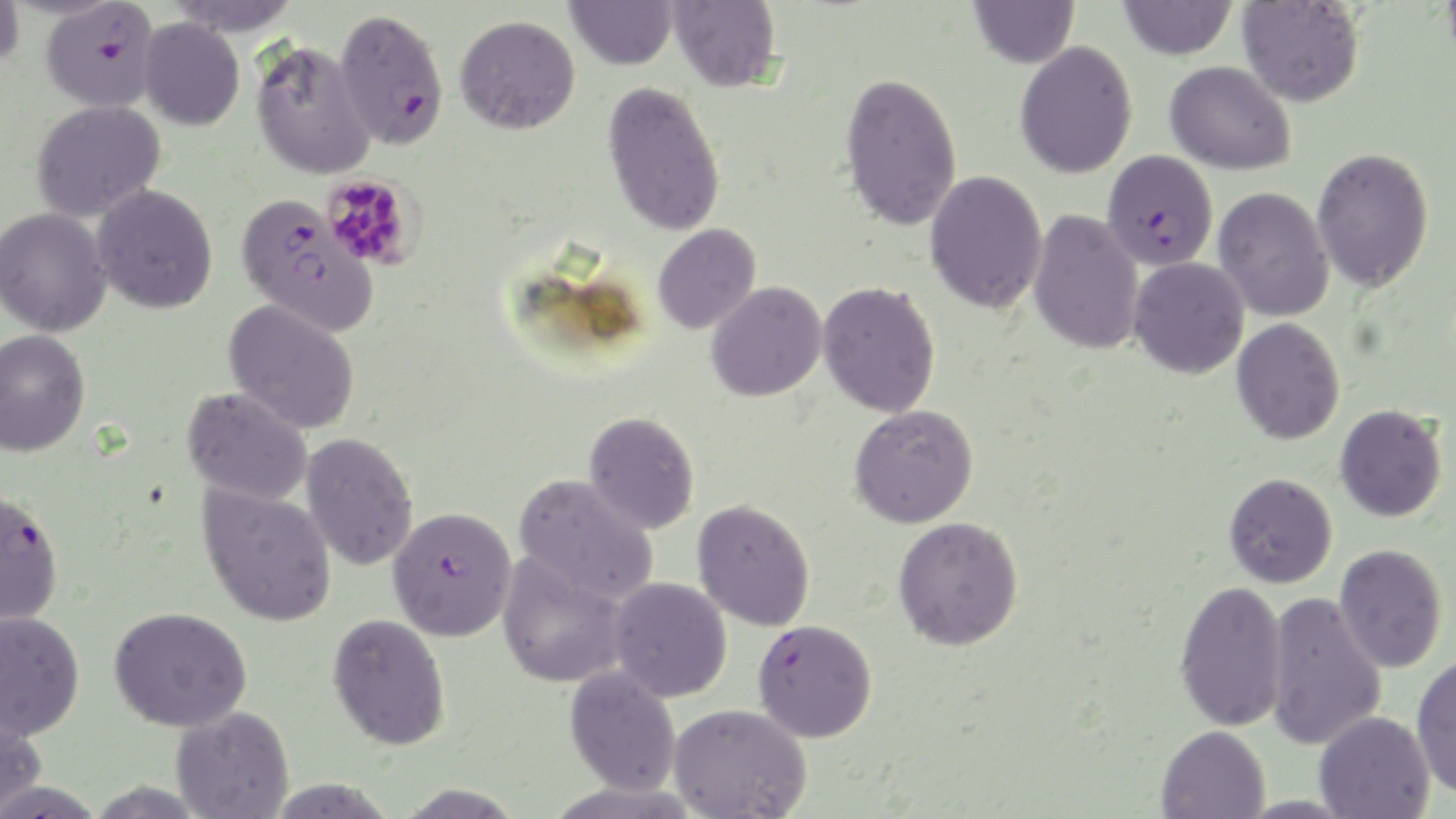
Approximate bounding boxes as named x1/y1/x2/y2 corners in pixels. Platelet locations: (x1=321, y1=174, x2=422, y2=271). Plasmodium falciparum-infected red blood cell locations: (x1=39, y1=1, x2=160, y2=113), (x1=334, y1=8, x2=449, y2=150), (x1=1102, y1=149, x2=1218, y2=271), (x1=235, y1=192, x2=376, y2=334), (x1=0, y1=486, x2=64, y2=627), (x1=387, y1=506, x2=518, y2=641), (x1=752, y1=618, x2=877, y2=742). Uninfected red blood cell locations: (x1=166, y1=0, x2=303, y2=36), (x1=565, y1=0, x2=678, y2=70), (x1=669, y1=0, x2=783, y2=92), (x1=968, y1=0, x2=1080, y2=68), (x1=1116, y1=0, x2=1238, y2=60), (x1=0, y1=1, x2=25, y2=72), (x1=1237, y1=1, x2=1365, y2=107), (x1=455, y1=15, x2=580, y2=135), (x1=139, y1=18, x2=244, y2=131), (x1=251, y1=41, x2=377, y2=180), (x1=1015, y1=41, x2=1138, y2=178), (x1=1165, y1=61, x2=1296, y2=175), (x1=839, y1=71, x2=962, y2=231), (x1=602, y1=81, x2=726, y2=237), (x1=30, y1=99, x2=166, y2=222), (x1=1311, y1=147, x2=1434, y2=293), (x1=925, y1=170, x2=1047, y2=314), (x1=92, y1=184, x2=218, y2=314), (x1=1213, y1=186, x2=1334, y2=322), (x1=0, y1=207, x2=112, y2=337), (x1=1028, y1=209, x2=1145, y2=355), (x1=652, y1=224, x2=761, y2=335), (x1=1128, y1=257, x2=1250, y2=379), (x1=705, y1=281, x2=826, y2=402), (x1=817, y1=281, x2=941, y2=417), (x1=223, y1=299, x2=361, y2=434), (x1=1231, y1=318, x2=1345, y2=445), (x1=0, y1=328, x2=90, y2=457), (x1=181, y1=388, x2=313, y2=506), (x1=850, y1=404, x2=978, y2=528), (x1=1334, y1=404, x2=1447, y2=522), (x1=583, y1=410, x2=700, y2=534), (x1=300, y1=432, x2=419, y2=571), (x1=1223, y1=472, x2=1337, y2=588), (x1=514, y1=473, x2=659, y2=606), (x1=197, y1=484, x2=337, y2=627), (x1=692, y1=499, x2=815, y2=631), (x1=893, y1=515, x2=1024, y2=650), (x1=1334, y1=543, x2=1448, y2=672), (x1=497, y1=552, x2=628, y2=688), (x1=609, y1=577, x2=732, y2=702), (x1=1174, y1=579, x2=1288, y2=732), (x1=1263, y1=590, x2=1387, y2=751), (x1=108, y1=606, x2=252, y2=732), (x1=0, y1=610, x2=85, y2=741), (x1=327, y1=613, x2=451, y2=751), (x1=1412, y1=653, x2=1456, y2=797), (x1=564, y1=664, x2=681, y2=796), (x1=0, y1=703, x2=46, y2=817), (x1=668, y1=703, x2=811, y2=819), (x1=171, y1=706, x2=294, y2=819), (x1=1314, y1=710, x2=1435, y2=819), (x1=1156, y1=725, x2=1270, y2=819). Slide-level diagnosis: Plasmodium falciparum. May-Grünwald-Giemsa-stained preparation. Light microscopy. Thin blood film. One field of a larger specimen. Image is 1456×819 pixels. Captured at 1000x magnification.